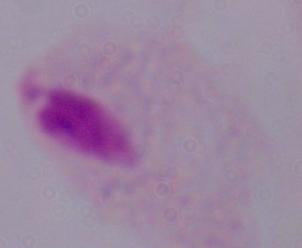 Photomicrograph. A trichomonad is shown. Captured at 1000x magnification.